Identify the cell.
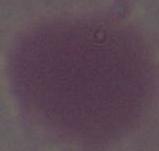
This is an erythrocyte.

Micrograph. Captured at 1000x magnification.